Name the parasite shown.
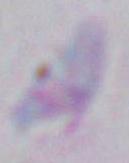
Toxoplasma gondii.

Captured at 1000x magnification. Photomicrograph.